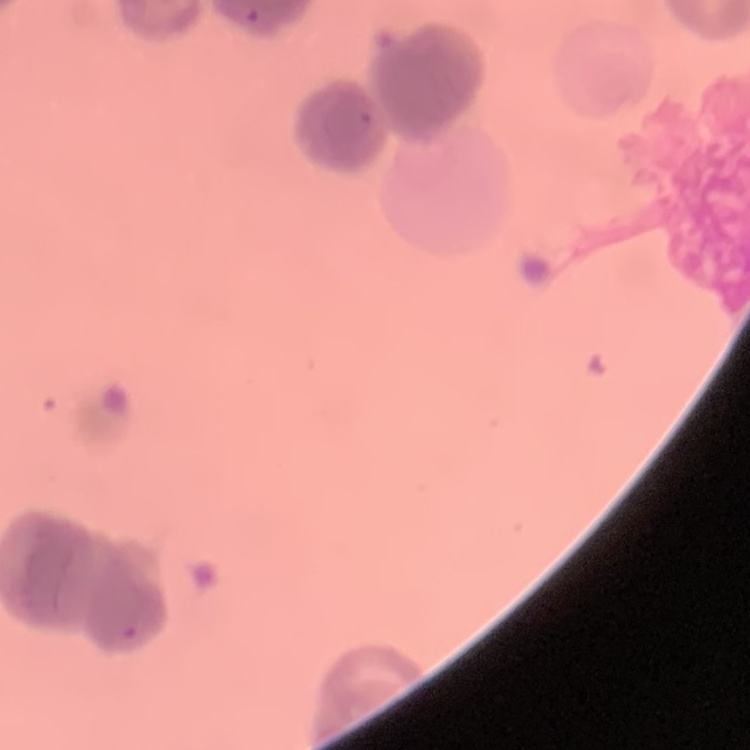

Summary:
  - Erythrocyte morphology: rouleaux formation
  - Stain: Field's or Giemsa
  - Preparation: thin peripheral smear
  - Image type: square crop of a larger photomicrograph